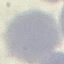

malaria status = uninfected
stain = Giemsa
image type = cell patch, automatically extracted from a larger field of view and resized to 64 × 64 pixels
capture = smartphone through the microscope eyepiece
preparation = thin blood film